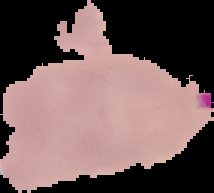
image_type: segmented cell region on a black background
malaria_status: uninfected
image_size: 214×193 pixels
preparation: thin blood film